Classify this cell by malaria status.
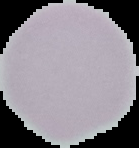

It is uninfected.

Image is 139×148 pixels. From a thin blood smear. Cell region segmented out of the field of view; the surrounding area is masked to black.